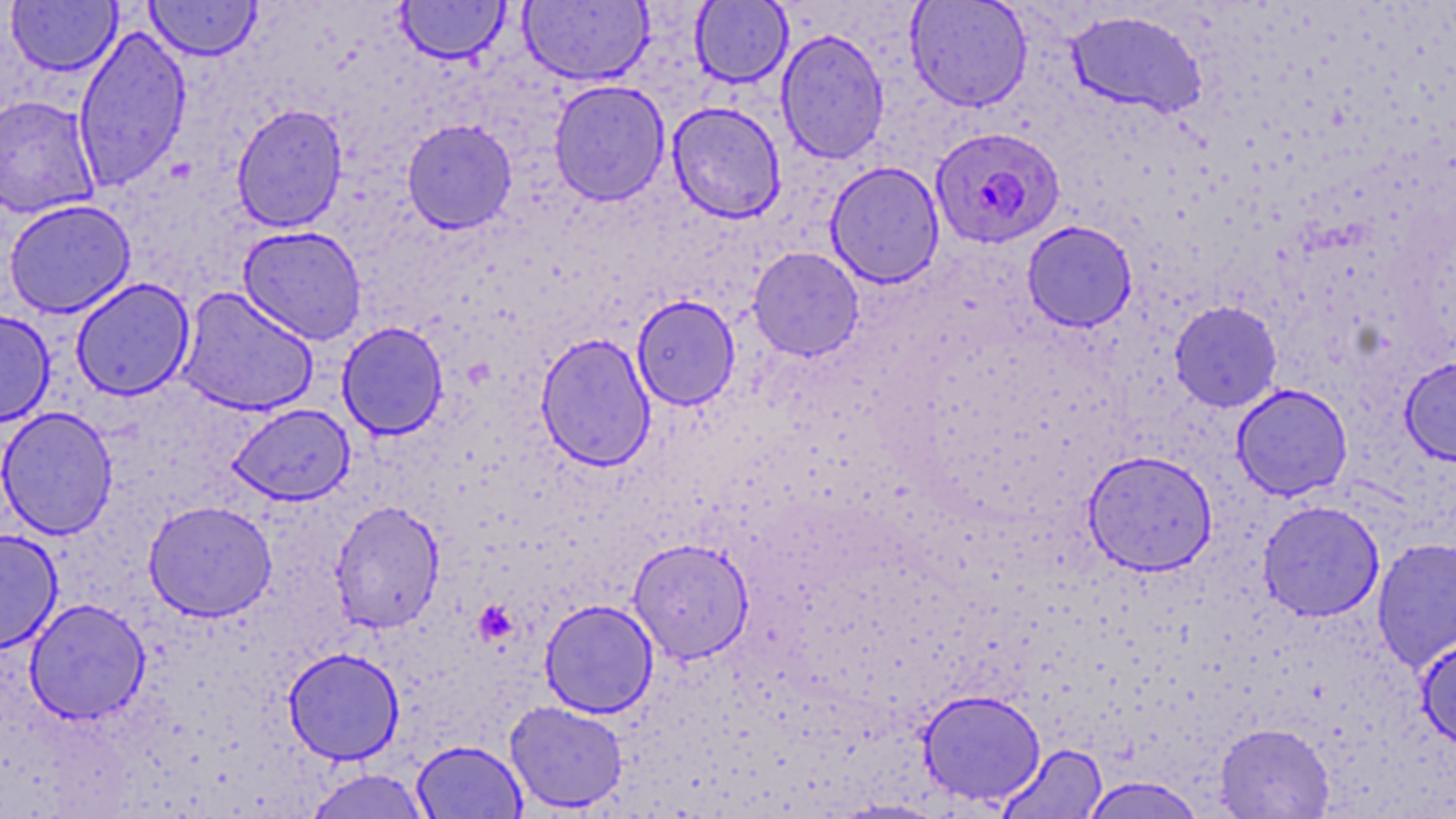

slide-level diagnosis = Plasmodium falciparum
preparation = thin blood smear
stain = May-Grünwald-Giemsa
image size = 1456×819 pixels
platelet locations = approximate bounding boxes as [x1, y1, x2, y2] in pixels: [473, 601, 517, 643]
modality = light microscopy
Plasmodium falciparum-infected red blood cell locations = approximate bounding boxes as [x1, y1, x2, y2] in pixels: [930, 126, 1066, 249]
uninfected red blood cell locations = approximate bounding boxes as [x1, y1, x2, y2] in pixels: [144, 0, 263, 61], [519, 0, 653, 86], [905, 0, 1033, 112], [6, 1, 121, 77], [395, 1, 511, 64], [691, 1, 793, 87], [1065, 9, 1207, 118], [73, 24, 192, 193], [776, 28, 889, 164], [548, 79, 670, 206], [0, 95, 101, 218], [666, 101, 786, 223], [231, 104, 349, 233], [402, 118, 518, 234], [825, 161, 945, 288], [3, 199, 136, 318], [1022, 220, 1138, 332], [238, 225, 368, 345], [748, 247, 864, 360], [70, 277, 195, 400], [176, 286, 320, 417], [632, 295, 740, 410], [1169, 301, 1283, 412], [0, 309, 55, 427], [336, 321, 449, 440], [534, 333, 656, 471], [1399, 356, 1456, 467], [1231, 383, 1353, 501], [227, 404, 355, 505], [1, 406, 119, 539], [1082, 449, 1218, 576], [143, 500, 278, 622], [330, 500, 445, 634], [1258, 500, 1385, 622], [0, 528, 63, 654], [1372, 537, 1456, 672], [628, 538, 755, 663], [24, 598, 150, 724], [539, 599, 659, 718], [1416, 634, 1456, 752], [282, 647, 404, 764], [918, 689, 1046, 806], [505, 701, 628, 813], [1215, 723, 1335, 818], [412, 739, 526, 819], [998, 743, 1108, 818], [303, 768, 432, 819], [1079, 776, 1207, 818], [831, 799, 950, 818]
field of view = single
magnification = 1000x